Assess this cell for malaria.
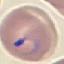

It is parasitized.

stain = Giemsa
image type = automatically extracted cell patch, resized to 64 × 64 pixels
capture = smartphone camera at the microscope eyepiece
preparation = thin blood smear